Comment on the morphology of the erythrocytes.
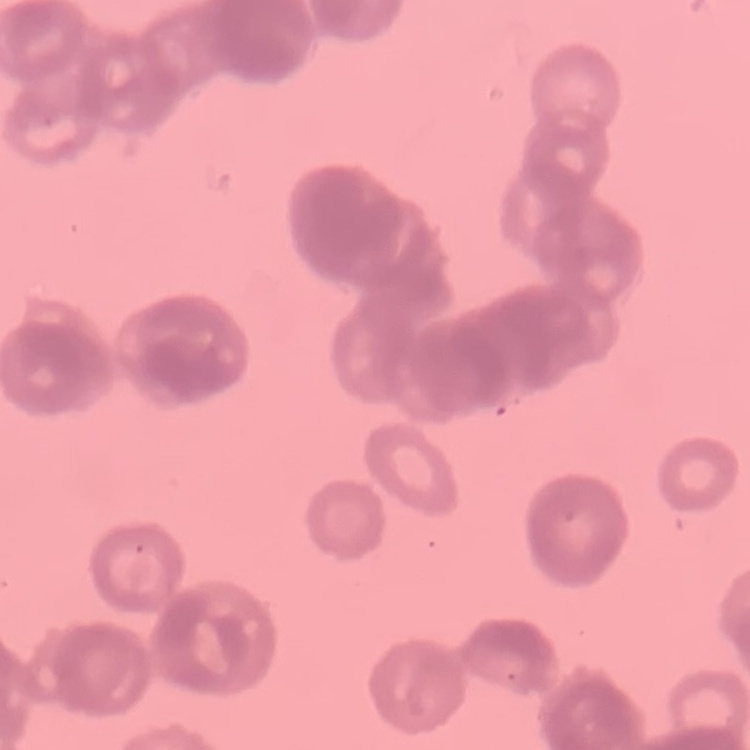

They show rouleaux formation.

Square crop of a larger photomicrograph. Thin blood smear. Field's or Giemsa stain.